Report the malaria status of this cell.
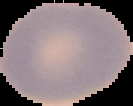

Uninfected.

{
  "image_size": "133×106 pixels",
  "image_type": "cell region segmented out of the field of view; surrounding area masked to black",
  "preparation": "thin blood smear"
}